Locate every uninfected red blood cell.
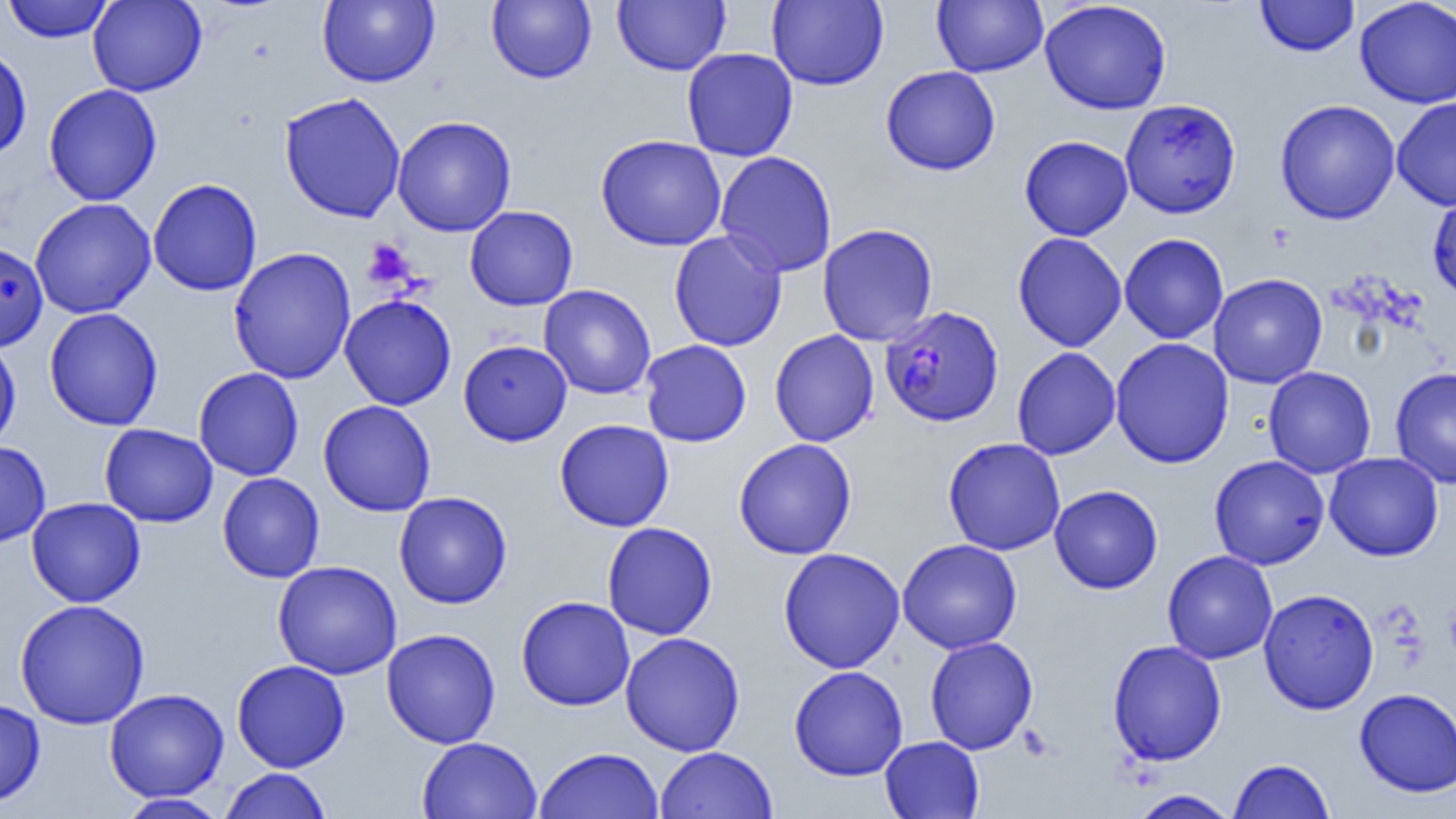

Approximate bounding boxes as named x1/y1/x2/y2 corners in pixels.
Uninfected red blood cells: (x1=87, y1=0, x2=206, y2=97), (x1=317, y1=0, x2=439, y2=87), (x1=486, y1=0, x2=597, y2=84), (x1=613, y1=0, x2=729, y2=75), (x1=767, y1=0, x2=888, y2=90), (x1=932, y1=0, x2=1048, y2=77), (x1=1255, y1=0, x2=1360, y2=57), (x1=1355, y1=0, x2=1456, y2=108), (x1=2, y1=1, x2=115, y2=43), (x1=1039, y1=1, x2=1172, y2=115), (x1=0, y1=45, x2=32, y2=161), (x1=681, y1=47, x2=798, y2=162), (x1=880, y1=66, x2=1001, y2=175), (x1=43, y1=84, x2=162, y2=206), (x1=279, y1=92, x2=407, y2=223), (x1=1392, y1=97, x2=1456, y2=210), (x1=1119, y1=98, x2=1241, y2=218), (x1=1275, y1=99, x2=1401, y2=224), (x1=392, y1=115, x2=516, y2=236), (x1=595, y1=134, x2=727, y2=251), (x1=1019, y1=135, x2=1133, y2=241), (x1=714, y1=150, x2=838, y2=278), (x1=148, y1=178, x2=263, y2=296), (x1=1427, y1=190, x2=1456, y2=302), (x1=30, y1=197, x2=156, y2=319), (x1=465, y1=205, x2=578, y2=310), (x1=817, y1=223, x2=938, y2=346), (x1=668, y1=230, x2=787, y2=351), (x1=1013, y1=232, x2=1127, y2=352), (x1=1119, y1=233, x2=1229, y2=344), (x1=0, y1=244, x2=48, y2=352), (x1=228, y1=247, x2=357, y2=384), (x1=1208, y1=273, x2=1328, y2=389), (x1=539, y1=284, x2=656, y2=399), (x1=339, y1=295, x2=457, y2=411), (x1=45, y1=307, x2=164, y2=431), (x1=769, y1=329, x2=879, y2=447), (x1=0, y1=337, x2=22, y2=453), (x1=1110, y1=337, x2=1235, y2=469), (x1=458, y1=339, x2=572, y2=446), (x1=639, y1=339, x2=752, y2=447), (x1=1011, y1=346, x2=1121, y2=460), (x1=1263, y1=366, x2=1377, y2=479), (x1=1390, y1=366, x2=1456, y2=489), (x1=193, y1=367, x2=304, y2=481), (x1=318, y1=399, x2=436, y2=517), (x1=554, y1=418, x2=674, y2=532), (x1=99, y1=423, x2=218, y2=527), (x1=942, y1=437, x2=1066, y2=556), (x1=733, y1=438, x2=858, y2=560), (x1=0, y1=441, x2=51, y2=548), (x1=1324, y1=452, x2=1443, y2=561), (x1=1208, y1=455, x2=1330, y2=570), (x1=217, y1=472, x2=325, y2=583), (x1=1049, y1=485, x2=1163, y2=594), (x1=394, y1=491, x2=512, y2=609), (x1=26, y1=497, x2=146, y2=607), (x1=601, y1=522, x2=717, y2=640), (x1=897, y1=539, x2=1022, y2=654), (x1=777, y1=547, x2=905, y2=673), (x1=1162, y1=550, x2=1278, y2=665), (x1=272, y1=560, x2=403, y2=680), (x1=1258, y1=588, x2=1379, y2=714), (x1=516, y1=595, x2=635, y2=711), (x1=14, y1=598, x2=150, y2=729), (x1=382, y1=629, x2=500, y2=749), (x1=620, y1=632, x2=746, y2=756), (x1=924, y1=635, x2=1038, y2=754), (x1=1107, y1=639, x2=1226, y2=766), (x1=231, y1=659, x2=350, y2=772), (x1=789, y1=665, x2=908, y2=781), (x1=104, y1=688, x2=230, y2=802), (x1=1354, y1=688, x2=1456, y2=797), (x1=0, y1=698, x2=46, y2=807), (x1=416, y1=736, x2=543, y2=818), (x1=880, y1=736, x2=985, y2=818), (x1=655, y1=746, x2=778, y2=819), (x1=534, y1=747, x2=664, y2=819), (x1=1228, y1=758, x2=1336, y2=818), (x1=220, y1=768, x2=331, y2=819), (x1=1128, y1=789, x2=1239, y2=818), (x1=115, y1=793, x2=230, y2=818).

Summary:
  - Platelet locations: (x1=363, y1=239, x2=415, y2=289), (x1=1444, y1=599, x2=1456, y2=662)
  - Plasmodium falciparum-infected red blood cell locations: (x1=879, y1=305, x2=1004, y2=427)
  - Slide-level diagnosis: Plasmodium falciparum
  - Modality: light microscopy
  - Preparation: thin blood film
  - Image size: 1456×819 pixels
  - Field of view: single
  - Magnification: 1000x